State the blood parasite species.
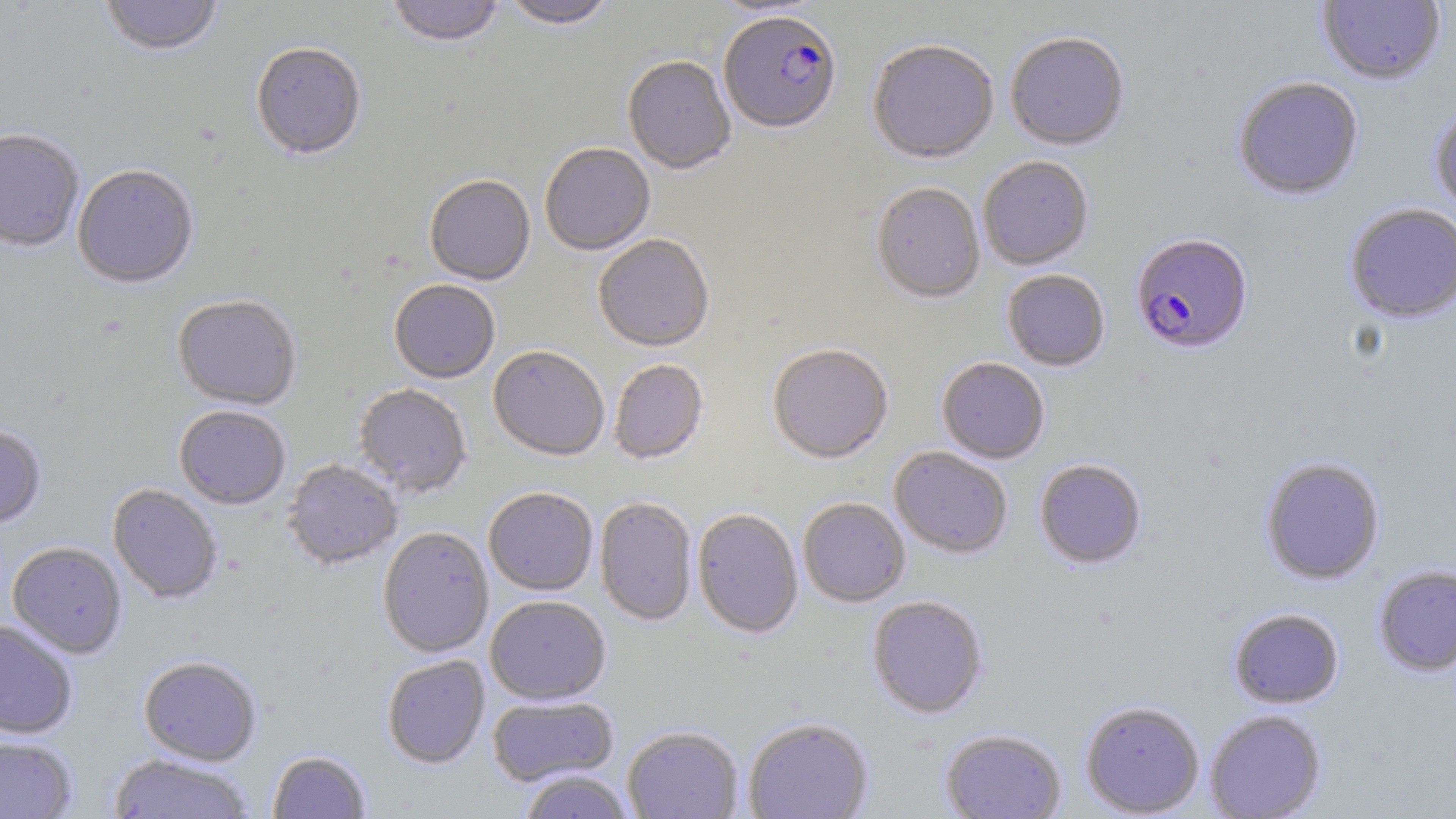

Plasmodium falciparum.

Approximate bounding boxes as (x1, y1, x2, y2) in pixels. Plasmodium falciparum-infected red blood cell locations: (719, 14, 841, 136), (1131, 235, 1253, 356). Uninfected red blood cell locations: (99, 0, 224, 59), (387, 0, 504, 50), (710, 0, 826, 19), (1317, 0, 1445, 87), (501, 1, 618, 33), (1005, 33, 1128, 152), (867, 42, 999, 166), (250, 45, 366, 163), (622, 58, 736, 177), (1233, 77, 1364, 201), (1430, 106, 1456, 215), (0, 131, 84, 255), (540, 145, 655, 257), (978, 158, 1093, 271), (72, 167, 199, 291), (424, 177, 535, 287), (871, 184, 985, 305), (1344, 204, 1456, 323), (593, 237, 714, 354), (1002, 270, 1110, 372), (389, 281, 500, 385), (172, 297, 302, 412), (767, 346, 893, 465), (488, 348, 609, 463), (937, 358, 1049, 464), (609, 361, 708, 465), (353, 385, 471, 498), (174, 407, 290, 510), (0, 426, 47, 530), (889, 447, 1012, 560), (1260, 458, 1385, 585), (282, 460, 403, 572), (1034, 460, 1147, 571), (108, 485, 222, 605), (484, 489, 598, 597), (594, 498, 697, 628), (798, 498, 910, 608), (692, 510, 803, 640), (377, 529, 494, 659), (7, 543, 127, 659), (1373, 565, 1456, 677), (486, 597, 610, 706), (867, 597, 988, 719), (1228, 608, 1344, 709), (0, 620, 78, 739), (381, 655, 490, 769), (138, 657, 261, 766), (487, 696, 619, 788), (1080, 701, 1205, 817), (1205, 710, 1326, 819), (743, 718, 874, 819), (622, 727, 743, 819), (941, 729, 1066, 819), (0, 736, 78, 818), (267, 751, 371, 818), (109, 754, 255, 819), (518, 771, 635, 819). Image is 1456×819 pixels. 1000x magnification. One field of a larger specimen. Thin blood smear. Optical microscopy. May-Grünwald-Giemsa-stained preparation.